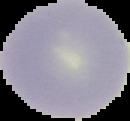
image size = 130×121 pixels
image type = segmented cell region on a black background
malaria status = uninfected
preparation = thin blood film